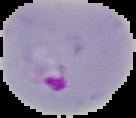

Summary:
  - Malaria status: parasitized
  - Image type: segmented cell region on a black background
  - Image size: 136×118 pixels
  - Preparation: thin blood film